Give the preparation type.
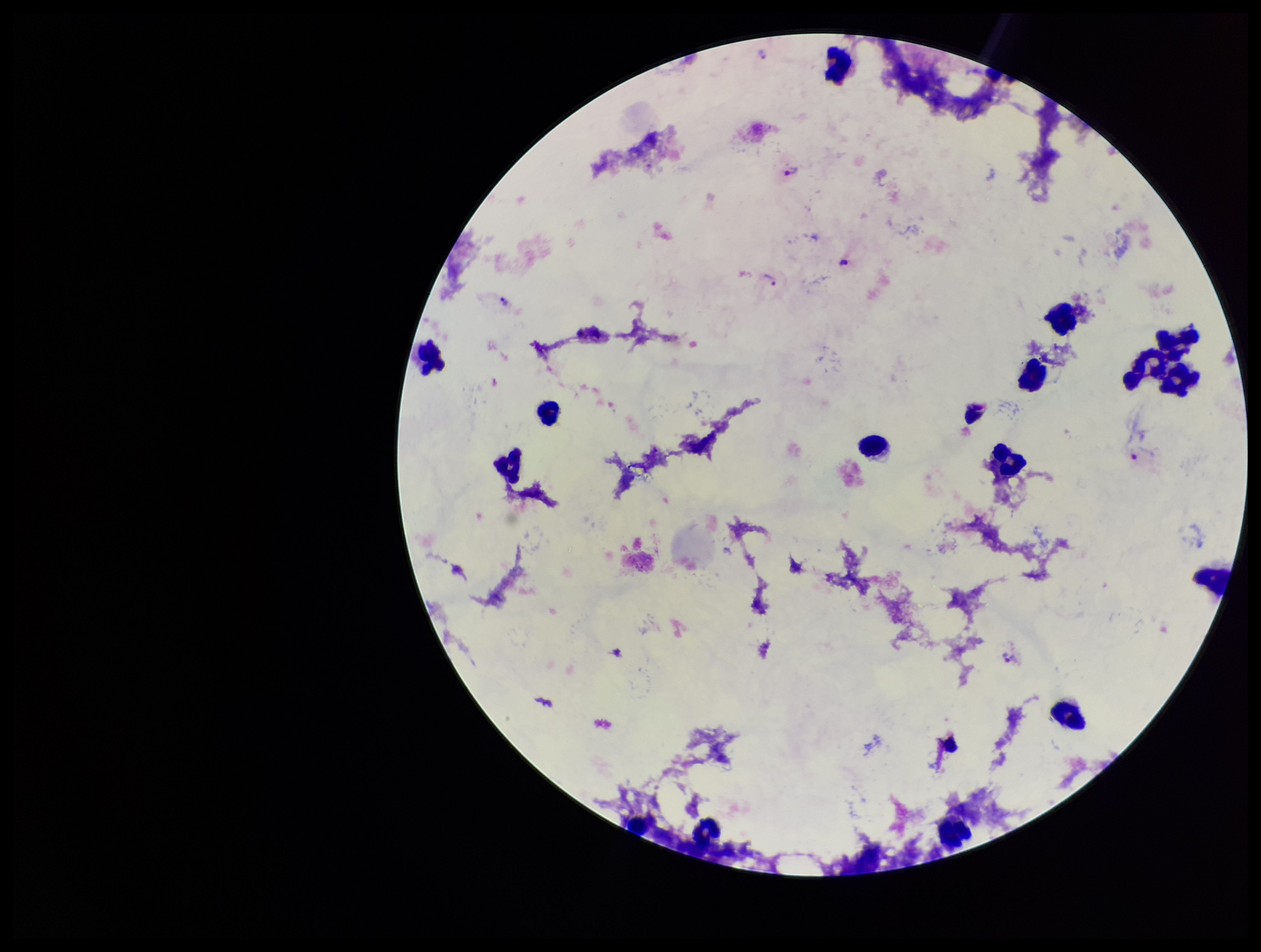

A thick smear.

Summary:
  - Species reported for this patient: Plasmodium vivax
  - Patient malaria status: positive
  - Image size: 1261×952 pixels
  - Leukocyte count: 16
  - Plasmodium parasites: seen
  - Field of view: one from this slide
  - Capture: smartphone photograph through the microscope eyepiece
  - Stain: Giemsa
  - Parasite count: 5